Point out every Plasmodium parasite.
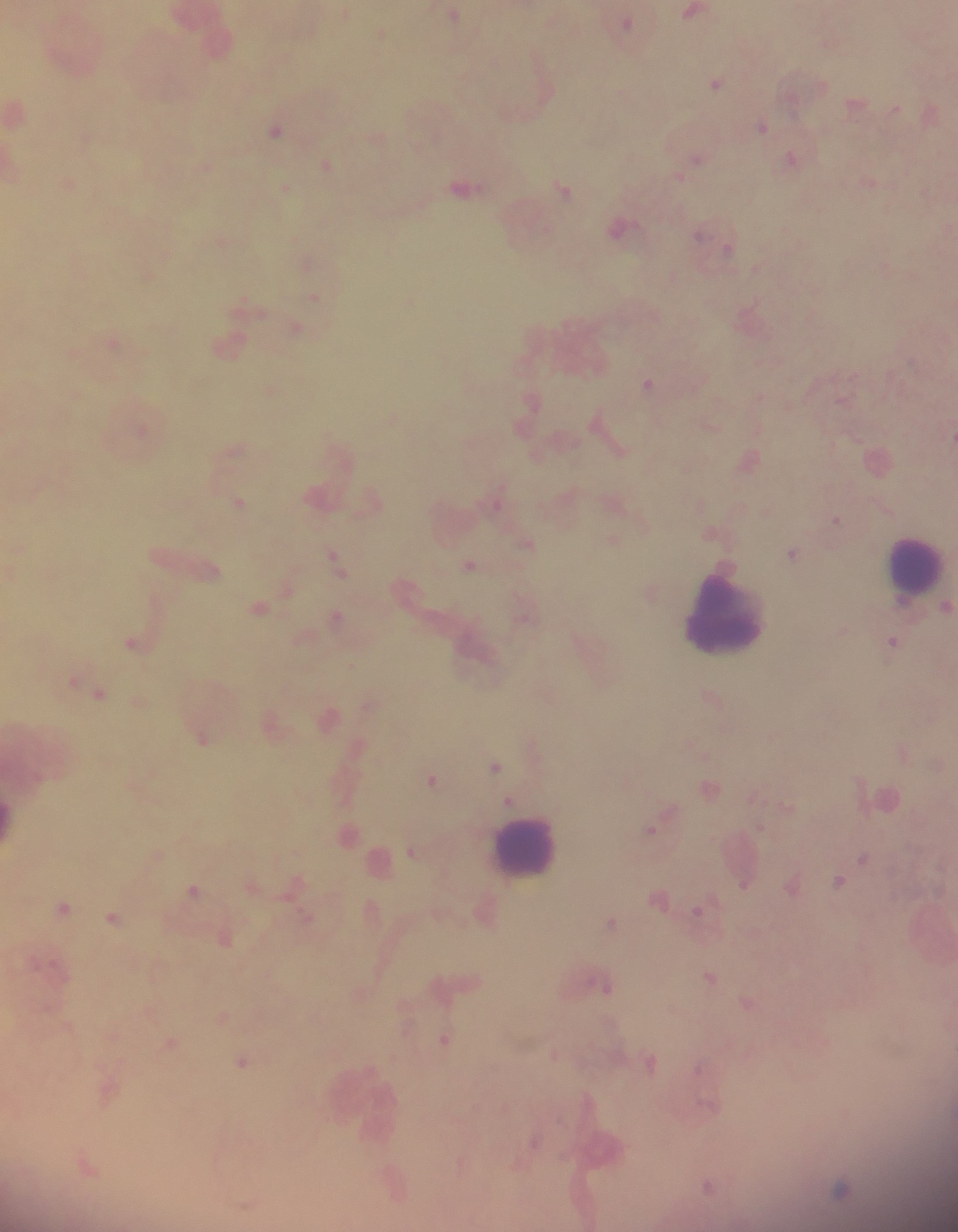
Approximate centers as [x, y] in pixels.
Plasmodium parasites: [692, 12], [346, 13], [454, 15], [626, 22], [380, 34], [717, 82], [855, 102], [896, 108], [15, 110], [763, 126], [275, 131], [792, 158], [696, 160], [205, 164], [325, 165], [868, 182], [68, 184], [464, 187], [285, 188], [563, 188], [619, 228], [700, 233], [728, 250], [756, 269], [315, 297], [296, 328], [113, 341], [648, 384], [271, 389], [141, 429], [236, 449], [750, 460], [498, 493], [240, 502], [836, 519], [613, 540], [527, 544], [793, 553], [335, 561], [469, 565], [211, 571], [947, 606], [259, 607], [336, 617], [892, 642], [134, 643], [74, 680], [99, 693], [329, 719], [203, 738], [532, 742], [359, 746], [903, 752], [495, 766], [431, 780], [709, 789], [509, 801], [651, 830], [411, 850], [864, 857], [839, 881], [295, 883], [745, 883], [791, 887], [194, 890], [659, 899], [64, 907], [699, 910], [112, 918], [307, 918], [611, 923], [225, 940], [709, 977], [602, 984], [747, 1002], [223, 1017], [445, 1040], [169, 1043], [243, 1061], [650, 1062], [700, 1067], [106, 1088], [708, 1105], [534, 1141], [708, 1186], [841, 1188].

image size = 958×1232 pixels
preparation = thick blood smear
leukocyte locations = approximate centers as [x, y] in pixels: [914, 567], [726, 615], [527, 848]
capture = mobile-phone photograph through a microscope
country = Ghana
field of view = single